Classify this cell by malaria status.
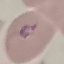
Parasitized.

{
  "capture": "smartphone camera at the microscope eyepiece",
  "image_type": "cell patch, automatically extracted from a larger field of view and resized to 64 × 64 pixels",
  "preparation": "thin blood film",
  "stain": "Giemsa"
}